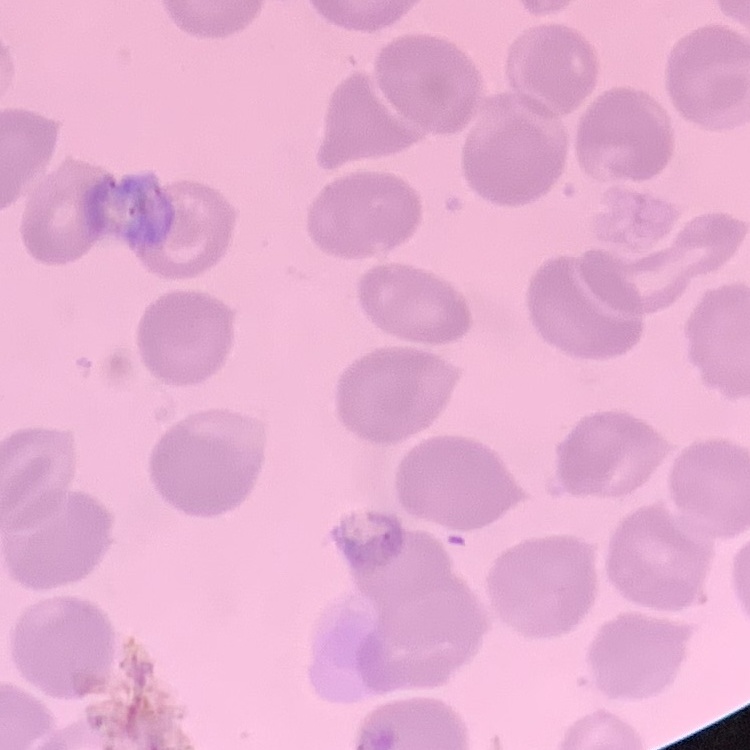

Summary:
  - Erythrocyte morphology: no rouleaux formation
  - Image type: one tile cut from a larger photomicrograph
  - Preparation: thin peripheral smear
  - Stain: Field's or Giemsa